Assess for Plasmodium parasites.
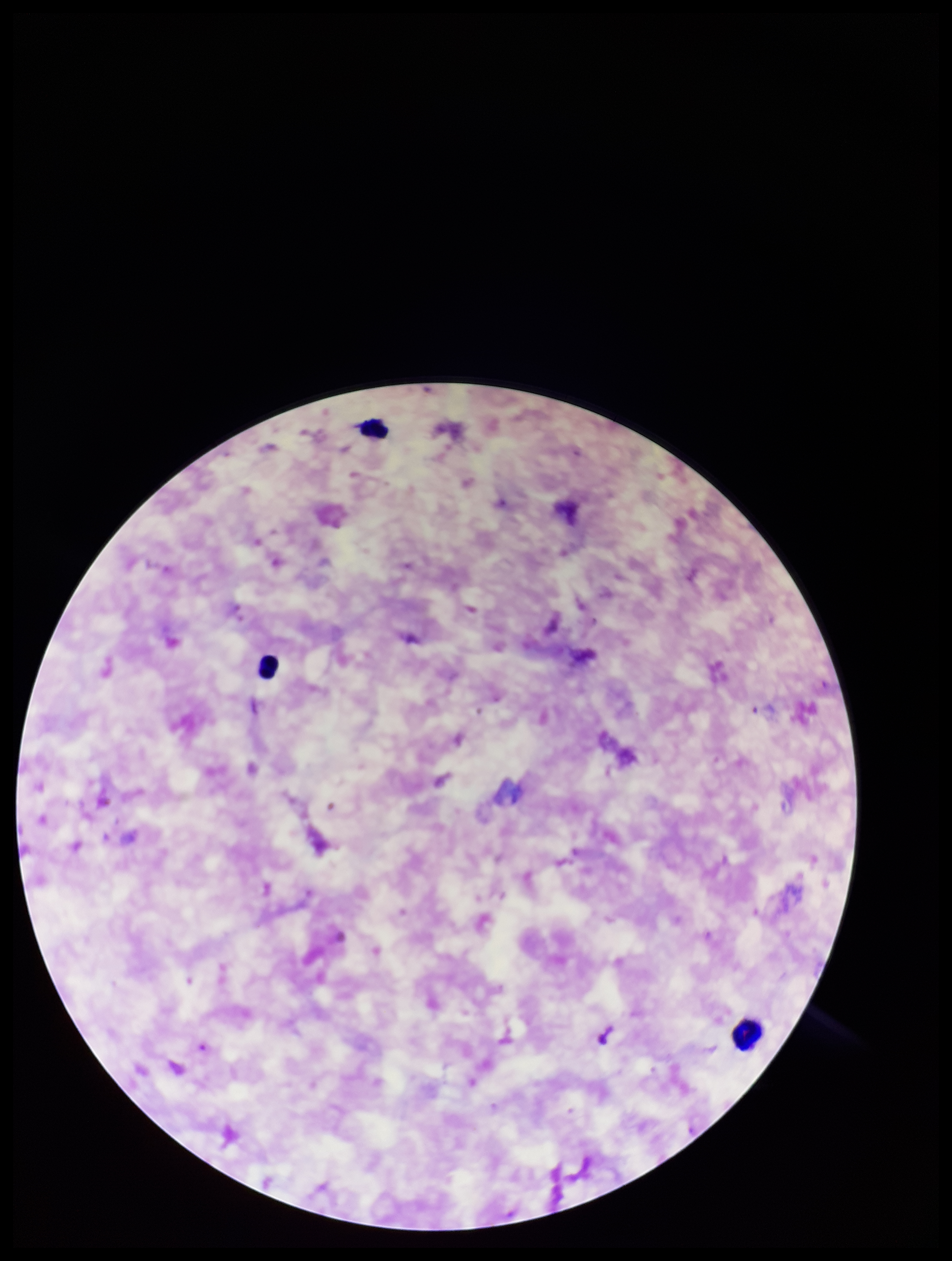

None detected.

Summary:
  - Parasite count: 0
  - Image size: 952×1261 pixels
  - Leukocyte count: 3
  - Patient malaria status: positive
  - Capture: smartphone photograph through the microscope eyepiece
  - Stain: Giemsa
  - Field of view: one from this slide
  - Species reported for this patient: Plasmodium falciparum
  - Preparation: thick smear